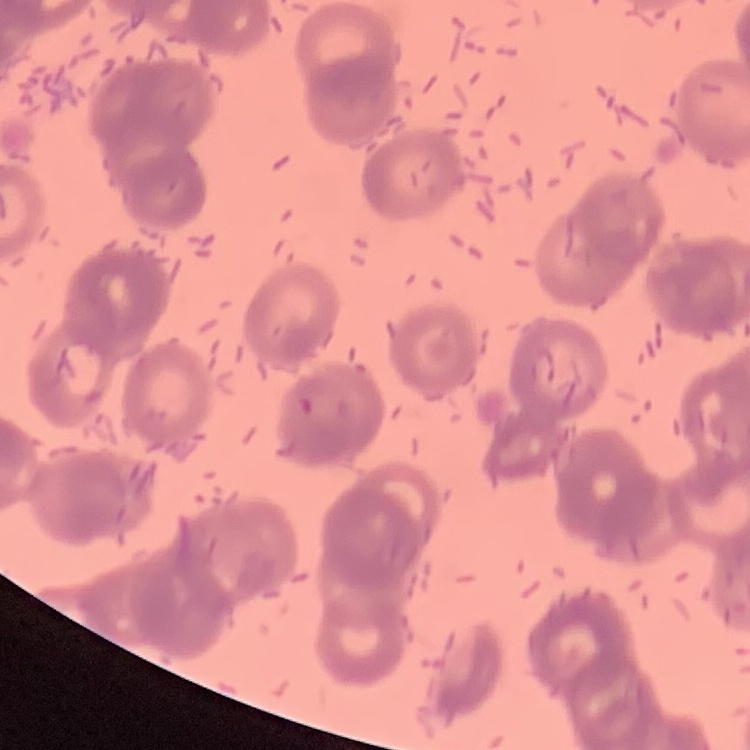

The red blood cells exhibit rouleaux formation. One tile cut from a larger photomicrograph. Thin blood film. Field's or Giemsa stain.